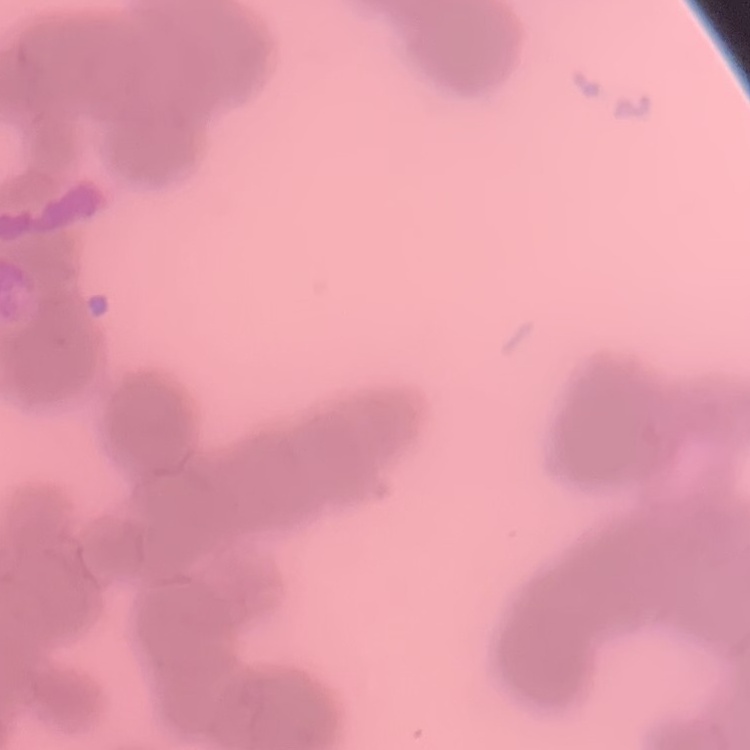
The erythrocytes exhibit rouleaux formation. One tile cut from a larger photomicrograph. Stained with either Field's or Giemsa. Thin blood film.